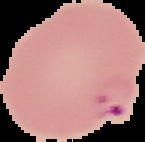

Image is 145×142 pixels. Result: malaria parasites identified. The area outside the segmented cell region is set to black. From a thin blood smear.